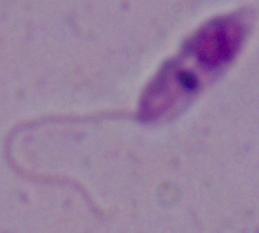 1000x magnification. A Leishmania parasite is shown. Photomicrograph.